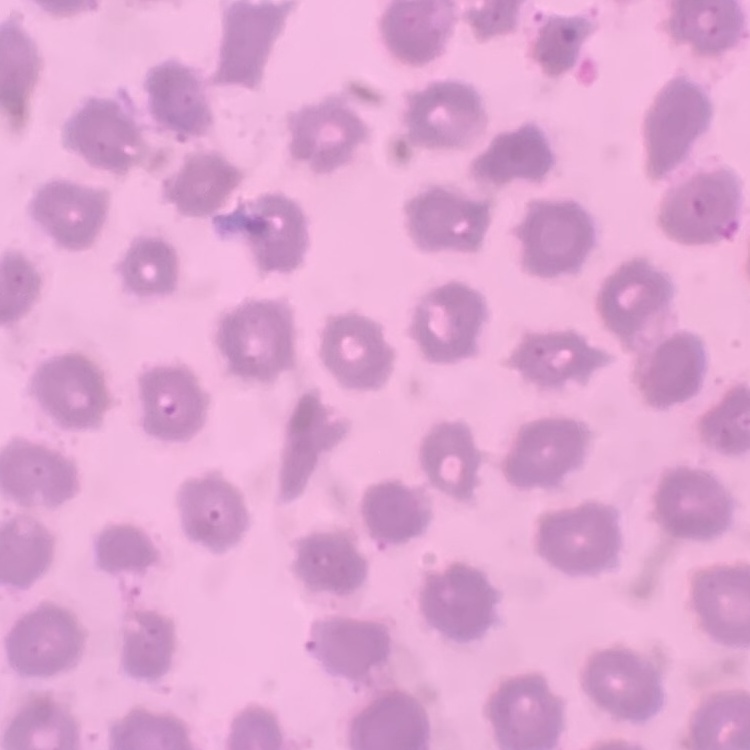
erythrocyte morphology = no rouleaux formation
image type = square crop of a larger photomicrograph
preparation = thin peripheral smear
stain = Field's or Giemsa